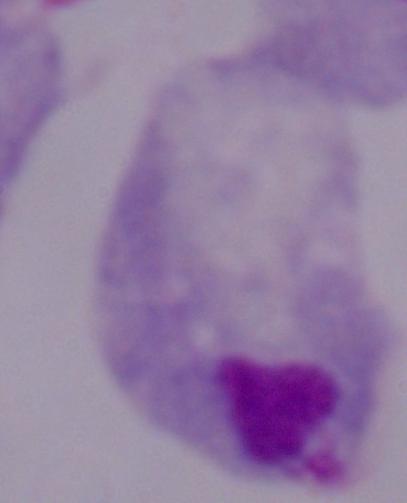 1000x magnification. A trichomonad is shown. Micrograph.